Identify the parasite.
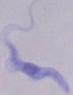
A trypanosome.

Captured at 1000x magnification. Photomicrograph.